Assess this cell for malaria.
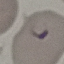

Parasitized.

Giemsa stain. Automatically extracted cell patch, resized to 64 × 64 pixels. Photographed with a smartphone camera at the microscope eyepiece. Thin blood film.